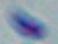
Summary:
  - Modality: photomicrograph
  - Magnification: 1000x
  - Identification: Toxoplasma gondii